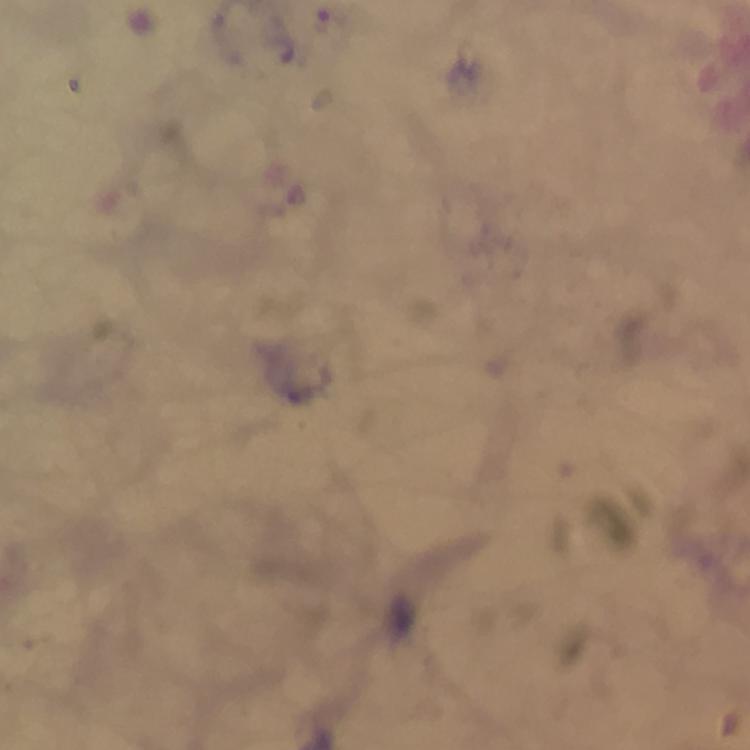
context = from a diagnostic examination for malaria
magnification = 100x
stain = Giemsa
image size = 750×750 pixels
capture = smartphone camera through the microscope
immersion oil = used
malaria parasite locations = approximate centers as {x, y} in pixels: {296, 195}
cropped from = a single field of view
preparation = thick smear